Assess the morphology of the red blood cells.
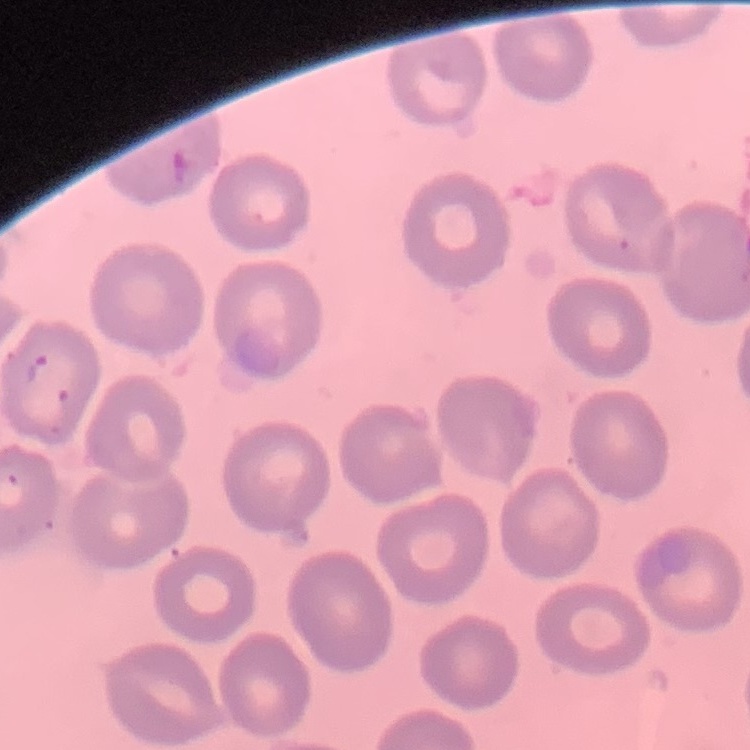
No rouleaux formation.

Field's or Giemsa stain. Thin blood smear. One tile cut from a larger photomicrograph.